State which cell type is depicted.
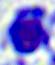

This is a leukocyte.

Micrograph. Captured at 400x magnification.